Classify this cell by malaria status.
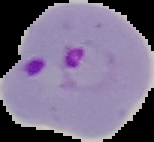
It is parasitized.

Summary:
  - Image size: 154×142 pixels
  - Preparation: thin blood film
  - Image type: segmented cell region on a black background